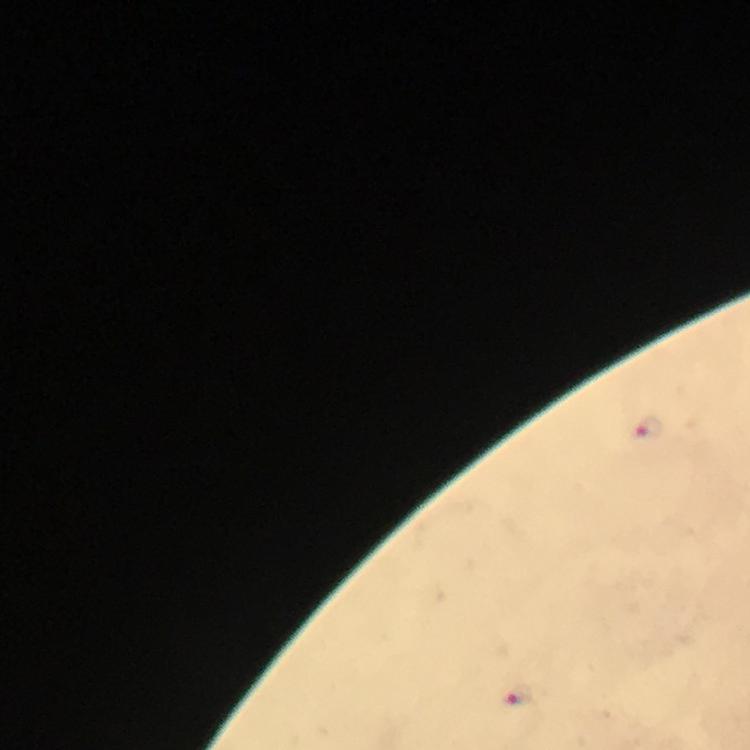

Approximate centers as [x, y] in pixels.
Summary:
  - Plasmodium parasite locations: [649, 428], [518, 695]
  - Image size: 750×750 pixels
  - Magnification: 100x
  - Preparation: thick smear
  - Immersion oil: applied
  - Stain: Giemsa
  - Context: from a diagnostic examination for malaria
  - Cropped from: a single field of view
  - Capture: smartphone camera through the microscope